Locate and identify every blood parasite.
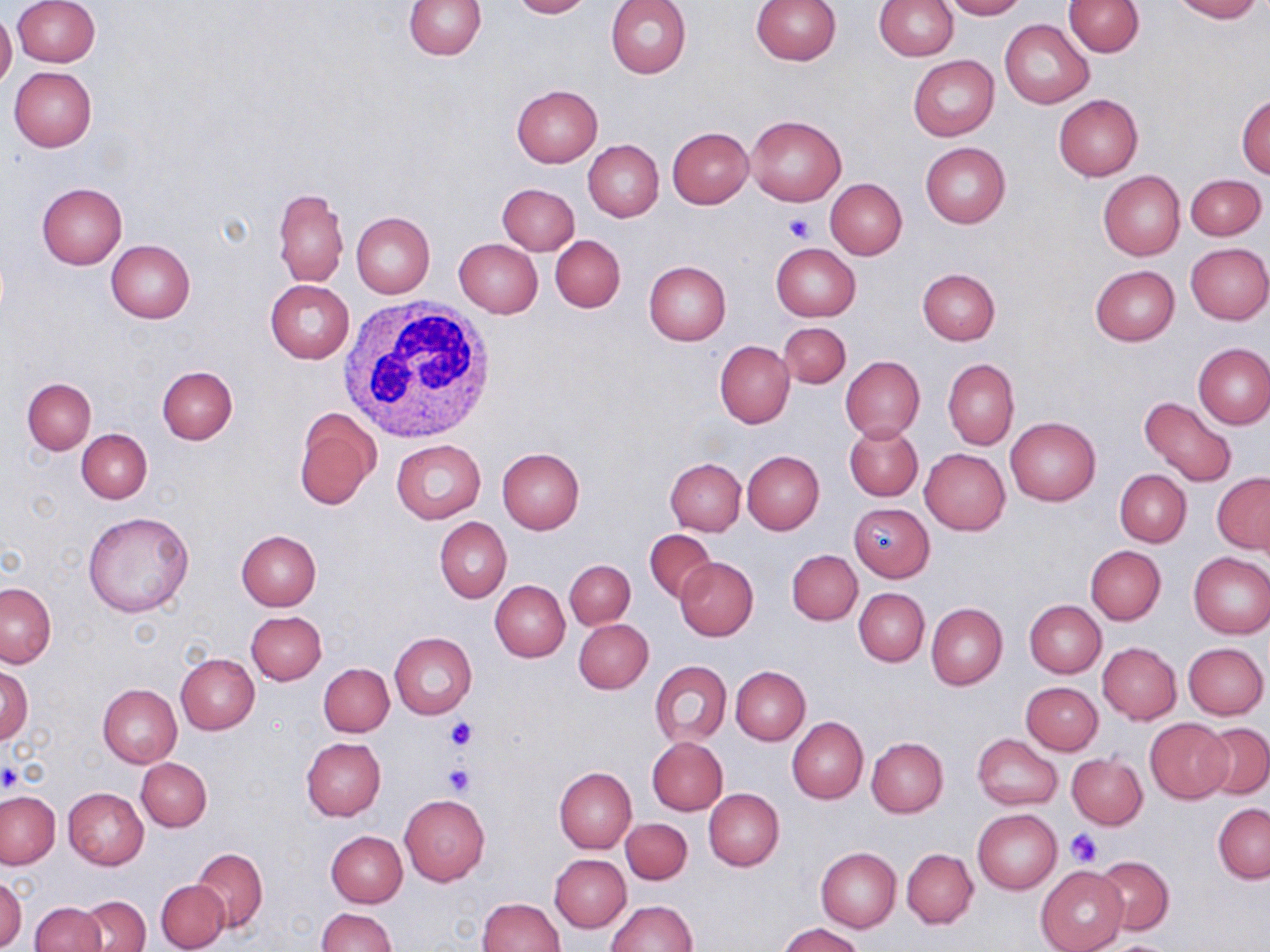

No blood parasites observed.

slide_level_diagnosis: negative for blood parasites
image_size: 1270×952 pixels
magnification: 1000x
uninfected_red_blood_cell_locations: 'approximate bounding boxes as [x1, y1, x2, y2] in pixels: [12, 0, 100, 66], [403, 0, 485, 59], [508, 0, 590, 18], [605, 0, 691, 79], [750, 0, 840, 66], [874, 0, 957, 60], [943, 0, 1026, 20], [1168, 0, 1261, 22], [1064, 1, 1143, 57], [0, 10, 17, 89], [1000, 20, 1093, 107], [908, 55, 998, 141], [9, 66, 96, 151], [512, 85, 603, 167], [1236, 94, 1270, 178], [1053, 95, 1143, 181], [746, 114, 846, 206], [668, 127, 753, 208], [583, 140, 663, 222], [920, 142, 1010, 228], [1098, 171, 1186, 260], [1187, 174, 1266, 240], [825, 179, 907, 259], [37, 183, 127, 268], [497, 183, 579, 254], [273, 186, 348, 286], [351, 212, 435, 297], [551, 236, 625, 312], [453, 238, 543, 318], [106, 239, 196, 323], [770, 243, 860, 321], [1185, 243, 1270, 324], [643, 261, 730, 346], [1089, 266, 1180, 346], [917, 268, 1000, 345], [265, 280, 354, 363], [779, 321, 851, 388], [715, 340, 794, 429], [1194, 343, 1270, 429], [840, 356, 925, 442], [942, 358, 1018, 450], [157, 367, 237, 445], [22, 378, 96, 454], [1138, 397, 1238, 486], [294, 408, 380, 511], [1005, 418, 1100, 507], [846, 424, 923, 501], [77, 429, 152, 503], [392, 439, 486, 523], [497, 448, 585, 533], [920, 448, 1010, 535], [743, 450, 824, 534], [665, 457, 746, 535], [1115, 469, 1191, 546], [1212, 473, 1270, 554], [849, 503, 934, 581], [82, 512, 194, 618], [434, 517, 510, 602], [236, 529, 322, 609], [645, 529, 716, 602], [1085, 545, 1166, 625], [787, 550, 862, 625], [1188, 551, 1270, 638], [676, 558, 758, 641], [564, 560, 635, 629], [490, 581, 569, 662], [0, 582, 55, 668], [854, 588, 929, 666], [1024, 600, 1106, 677], [926, 603, 1007, 690], [246, 611, 326, 685], [574, 618, 653, 693], [390, 632, 476, 720], [1098, 642, 1181, 724], [1184, 642, 1268, 719], [176, 654, 259, 734], [650, 660, 732, 746], [319, 664, 394, 737], [1, 665, 32, 744], [731, 665, 811, 744], [1021, 682, 1102, 754], [97, 684, 181, 767], [787, 716, 868, 803], [1145, 719, 1232, 802], [1199, 724, 1270, 799], [974, 734, 1063, 811], [646, 737, 728, 815], [867, 737, 949, 818], [302, 738, 386, 821], [1067, 753, 1147, 828], [137, 757, 211, 831], [554, 766, 637, 853], [63, 787, 148, 869], [704, 788, 784, 871], [0, 791, 60, 869], [399, 794, 490, 885], [1213, 803, 1270, 883], [973, 809, 1062, 894], [620, 818, 693, 884], [327, 831, 408, 906], [816, 846, 900, 933], [190, 847, 268, 933], [903, 848, 978, 928], [550, 854, 631, 932], [1093, 855, 1174, 935], [1036, 866, 1128, 952], [1, 875, 27, 950], [156, 879, 229, 952], [79, 894, 149, 952], [477, 898, 564, 952], [604, 900, 697, 952], [30, 902, 106, 952], [316, 907, 395, 952], [778, 922, 867, 952]'
platelet_locations: 'approximate bounding boxes as [x1, y1, x2, y2] in pixels: [783, 213, 815, 242], [444, 715, 479, 751], [442, 761, 475, 795], [0, 762, 23, 793], [1065, 829, 1103, 866]'
white_blood_cell_locations: 'approximate bounding boxes as [x1, y1, x2, y2] in pixels: [334, 299, 503, 440]'
field_of_view: one of a larger specimen
stain: May-Grünwald-Giemsa
preparation: thin blood smear
modality: optical microscopy